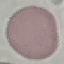
Malaria status: uninfected. Giemsa-stained preparation. Thin blood film. Cell patch, automatically extracted from a larger field of view and resized to 64 × 64 pixels. Photographed with a smartphone camera at the microscope eyepiece.